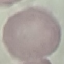

Result: no malaria parasites seen. Giemsa-stained preparation. Acquired by smartphone through the microscope eyepiece. Cell patch, automatically extracted from a larger field of view and resized to 64 × 64 pixels. Thin smear of blood.